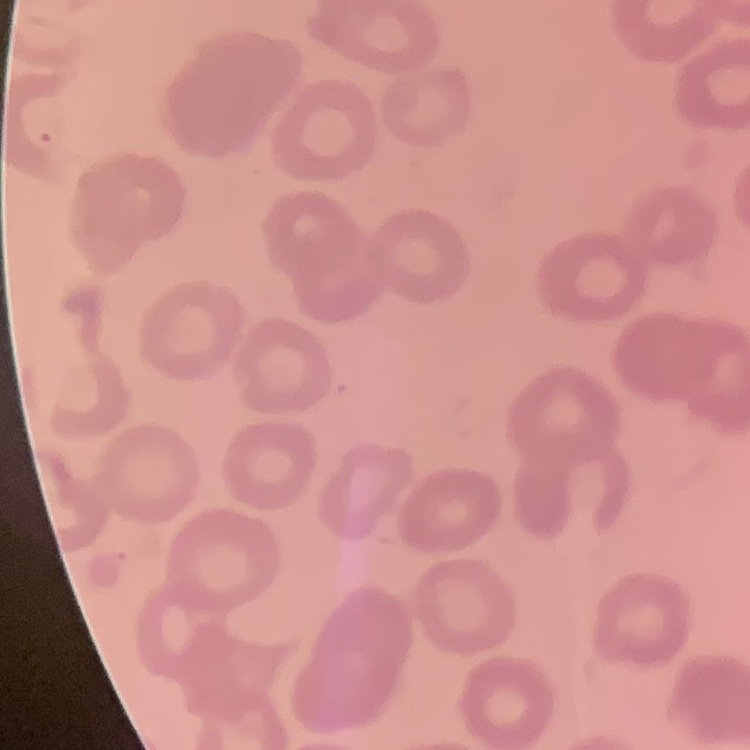
erythrocyte morphology = no rouleaux formation
preparation = thin blood film
stain = Field's or Giemsa
image type = square crop of a larger photomicrograph